Locate every uninfected red blood cell.
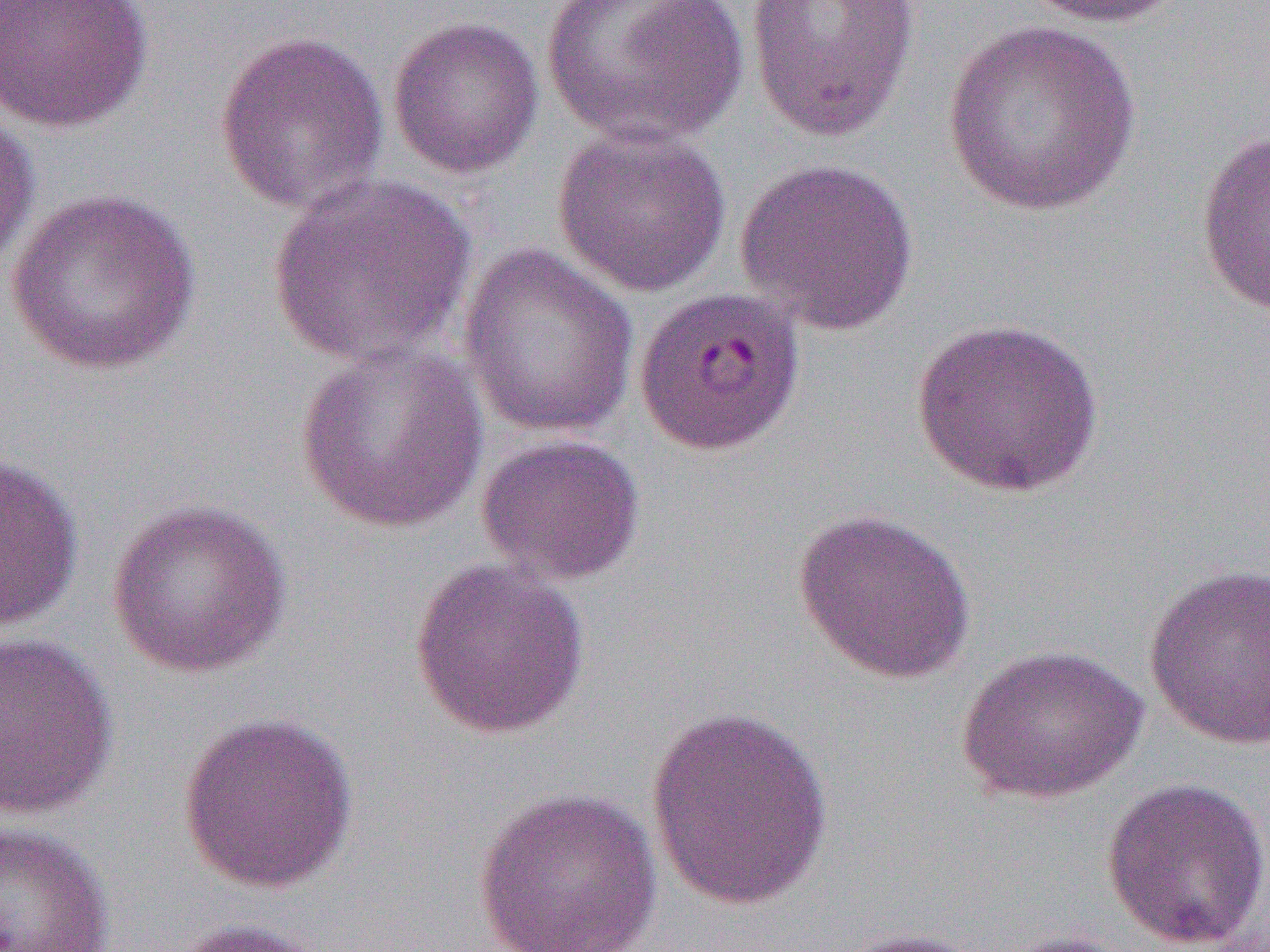

Approximate bounding boxes as [x1, y1, x2, y2] in pixels.
Uninfected red blood cells: [0, 0, 154, 134], [540, 0, 750, 147], [745, 0, 920, 143], [1017, 0, 1188, 28], [387, 15, 545, 180], [942, 20, 1142, 218], [214, 29, 390, 216], [0, 106, 40, 273], [552, 123, 732, 298], [1196, 128, 1270, 319], [734, 157, 921, 336], [267, 173, 477, 368], [5, 186, 203, 376], [458, 243, 639, 438], [911, 317, 1105, 497], [294, 340, 490, 535], [475, 433, 646, 586], [0, 455, 84, 632], [106, 499, 292, 678], [793, 508, 976, 685], [409, 558, 591, 739], [1144, 563, 1270, 750], [0, 631, 120, 819], [955, 643, 1149, 804], [644, 705, 834, 910], [176, 711, 359, 894], [1100, 775, 1270, 951], [472, 786, 662, 952], [0, 819, 116, 952], [166, 916, 333, 952], [827, 927, 994, 952], [990, 929, 1145, 952].

slide-level diagnosis = Plasmodium falciparum
field of view = one of a larger specimen
modality = optical microscopy
preparation = thin blood smear
image size = 1270×952 pixels
magnification = 1000x